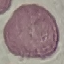

Malaria status: uninfected. Thin blood smear. Giemsa stain. Cell patch, automatically extracted from a larger field of view and resized to 64 × 64 pixels. Photographed with a smartphone camera at the microscope eyepiece.